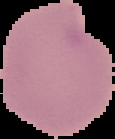

Summary:
  - Preparation: thin blood smear
  - Result: negative for malaria parasites
  - Image size: 115×139 pixels
  - Image type: segmented cell region with the area outside set to black